Name the blood parasite species.
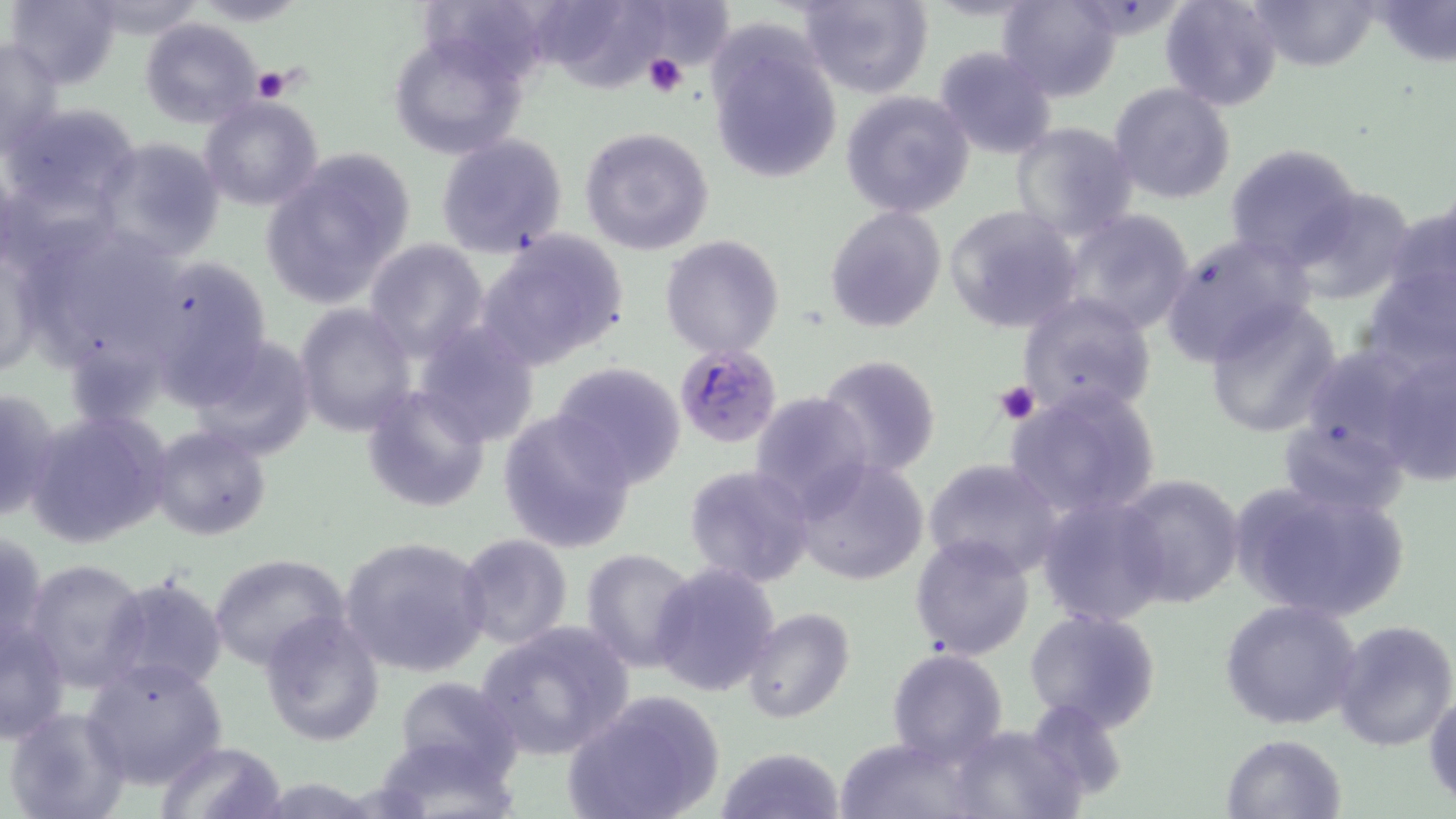
Plasmodium falciparum.

Approximate bounding boxes as (x1,y1)-(x2,y2) corner pairs in pixels. Uninfected red blood cell locations: (7,0)-(124,90), (418,0)-(555,85), (552,0)-(665,103), (799,0)-(932,98), (999,0)-(1124,102), (1159,0)-(1285,111), (1243,0)-(1382,71), (1374,0)-(1454,67), (83,1)-(205,41), (645,2)-(731,64), (141,18)-(265,128), (705,22)-(844,186), (386,27)-(534,162), (1,38)-(66,157), (933,45)-(1058,162), (1108,82)-(1236,205), (841,89)-(976,217), (198,95)-(326,212), (7,104)-(140,214), (1010,121)-(1140,243), (577,126)-(716,256), (434,133)-(570,260), (95,137)-(228,262), (1224,141)-(1363,269), (261,148)-(417,309), (1287,184)-(1419,304), (1385,200)-(1455,320), (824,205)-(947,333), (943,205)-(1083,334), (1058,208)-(1199,338), (25,222)-(183,367), (478,231)-(631,369), (1160,232)-(1311,366), (0,234)-(48,383), (660,234)-(784,358), (363,237)-(491,360), (136,252)-(274,397), (1356,265)-(1454,380), (1014,292)-(1158,420), (1201,299)-(1342,438), (295,302)-(419,437), (414,320)-(542,446), (187,335)-(318,461), (1374,344)-(1455,483), (1294,346)-(1435,469), (819,354)-(942,476), (549,361)-(688,488), (0,383)-(58,525), (361,384)-(492,513), (1003,384)-(1163,522), (749,390)-(875,515), (27,409)-(172,548), (499,411)-(637,554), (1277,416)-(1409,517), (150,424)-(272,543), (922,457)-(1065,579), (791,458)-(929,587), (683,464)-(814,587), (1115,473)-(1246,611), (1226,478)-(1412,624), (1035,494)-(1170,627), (0,528)-(48,655), (457,534)-(574,653), (910,535)-(1035,661), (340,536)-(492,676), (578,547)-(700,672), (208,554)-(352,673), (24,558)-(152,691), (649,561)-(781,699), (104,574)-(228,697), (1220,599)-(1362,730), (740,608)-(854,726), (1023,608)-(1165,734), (258,611)-(385,746), (0,617)-(71,743), (476,620)-(634,761), (1331,620)-(1456,753), (887,648)-(1010,766), (82,657)-(228,790), (392,675)-(522,790), (565,690)-(726,819), (1424,690)-(1456,806), (1026,695)-(1128,803), (4,706)-(131,819), (947,725)-(1077,817), (1220,732)-(1348,819), (833,735)-(979,819), (154,741)-(289,819), (717,746)-(845,819). Plasmodium falciparum-infected red blood cell locations: (674,342)-(781,448). Platelet locations: (643,53)-(689,98), (249,65)-(294,102), (994,380)-(1041,425). Image is 1456×819 pixels. Optical microscopy. May-Grünwald-Giemsa stain. Thin blood smear. One field of a larger specimen. 1000x magnification.